Name the parasite shown.
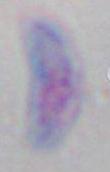

This is Toxoplasma gondii.

{
  "modality": "micrograph",
  "magnification": "1000x"
}